Identify the cell.
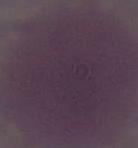
This is an erythrocyte.

modality = micrograph
magnification = 1000x